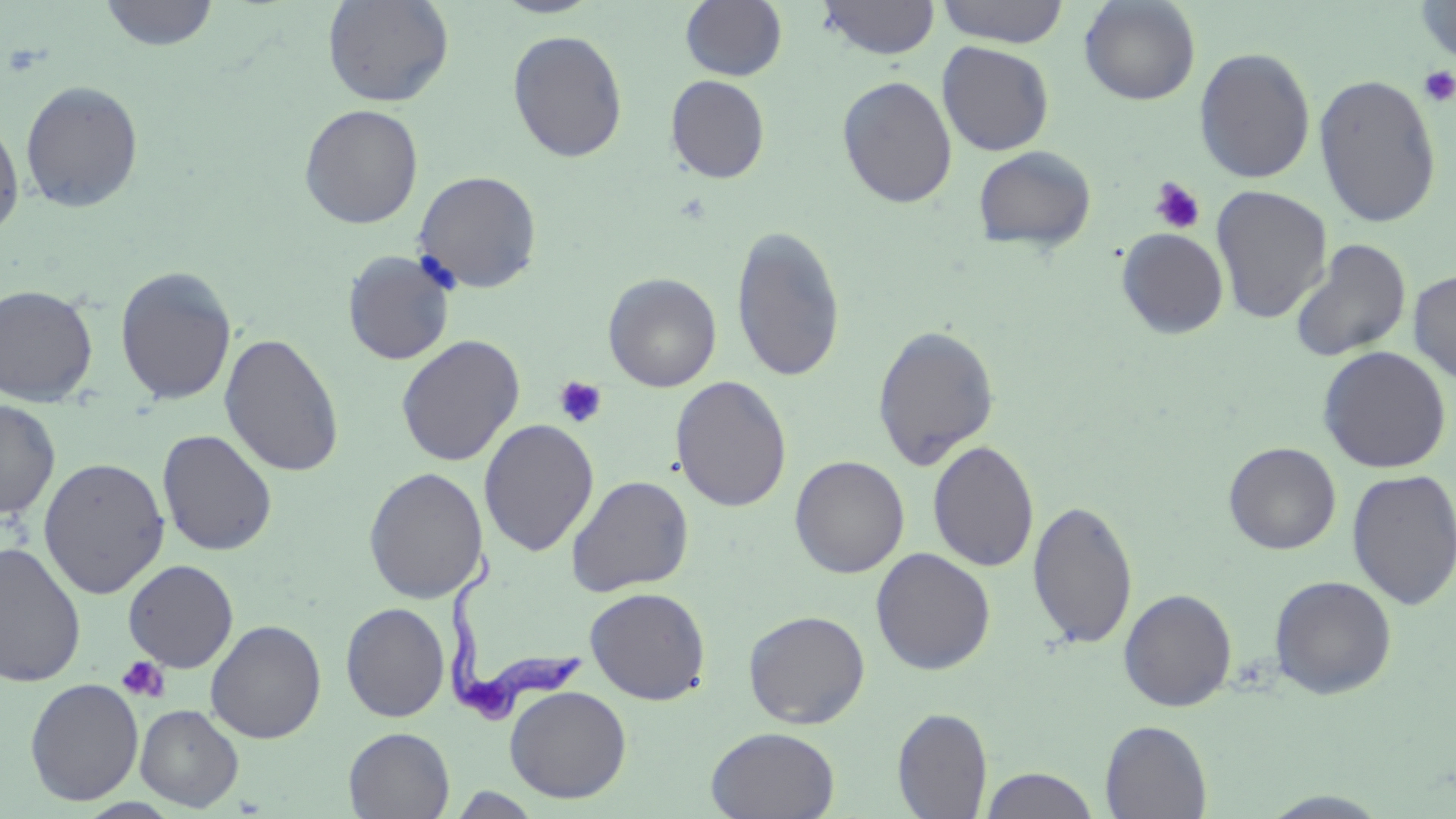
slide-level diagnosis = Trypanosoma brucei
field of view = one of a larger specimen
image size = 1456×819 pixels
Trypanosoma brucei locations = approximate bounding boxes as (x1,y1)-(x2,y2) corner pairs in pixels: (441,553)-(585,724)
modality = light microscopy
preparation = thin blood smear
magnification = 1000x
uninfected red blood cell locations = approximate bounding boxes as (x1,y1)-(x2,y2) corner pairs in pixels: (323,0)-(454,107), (493,0)-(604,18), (679,0)-(787,82), (817,0)-(939,60), (935,0)-(1070,47), (1414,0)-(1456,64), (98,1)-(220,51), (1079,1)-(1201,105), (507,30)-(628,163), (937,41)-(1054,156), (1194,46)-(1316,184), (1314,72)-(1442,228), (665,75)-(770,184), (837,75)-(957,209), (20,80)-(144,214), (299,104)-(423,229), (0,113)-(25,238), (972,145)-(1096,252), (413,170)-(543,294), (1211,185)-(1332,325), (731,224)-(847,383), (1116,228)-(1229,339), (1289,238)-(1412,364), (342,251)-(456,365), (115,266)-(237,405), (1407,269)-(1456,384), (603,272)-(722,392), (0,284)-(98,406), (872,323)-(1000,470), (219,333)-(344,477), (395,335)-(525,467), (1317,346)-(1452,474), (670,375)-(792,512), (0,400)-(60,519), (479,419)-(599,556), (157,429)-(277,556), (927,439)-(1040,574), (1223,442)-(1341,555), (790,455)-(909,578), (38,457)-(170,599), (363,467)-(488,604), (1346,468)-(1456,611), (566,475)-(694,597), (1027,498)-(1138,650), (0,541)-(86,689), (870,548)-(996,675), (123,559)-(239,672), (1268,574)-(1397,699), (585,587)-(711,705), (1119,589)-(1236,711), (341,602)-(450,722), (743,610)-(870,728), (205,620)-(326,743), (25,678)-(144,805), (504,685)-(632,803), (135,704)-(244,812), (892,707)-(992,818), (1100,720)-(1212,818), (706,726)-(840,818), (343,727)-(455,818), (980,768)-(1101,818), (1258,790)-(1394,818)
stain = May-Grünwald-Giemsa
platelet locations = approximate bounding boxes as (x1,y1)-(x2,y2) corner pairs in pixels: (1419,66)-(1456,108), (1149,177)-(1205,235), (553,376)-(608,429), (117,656)-(170,703)